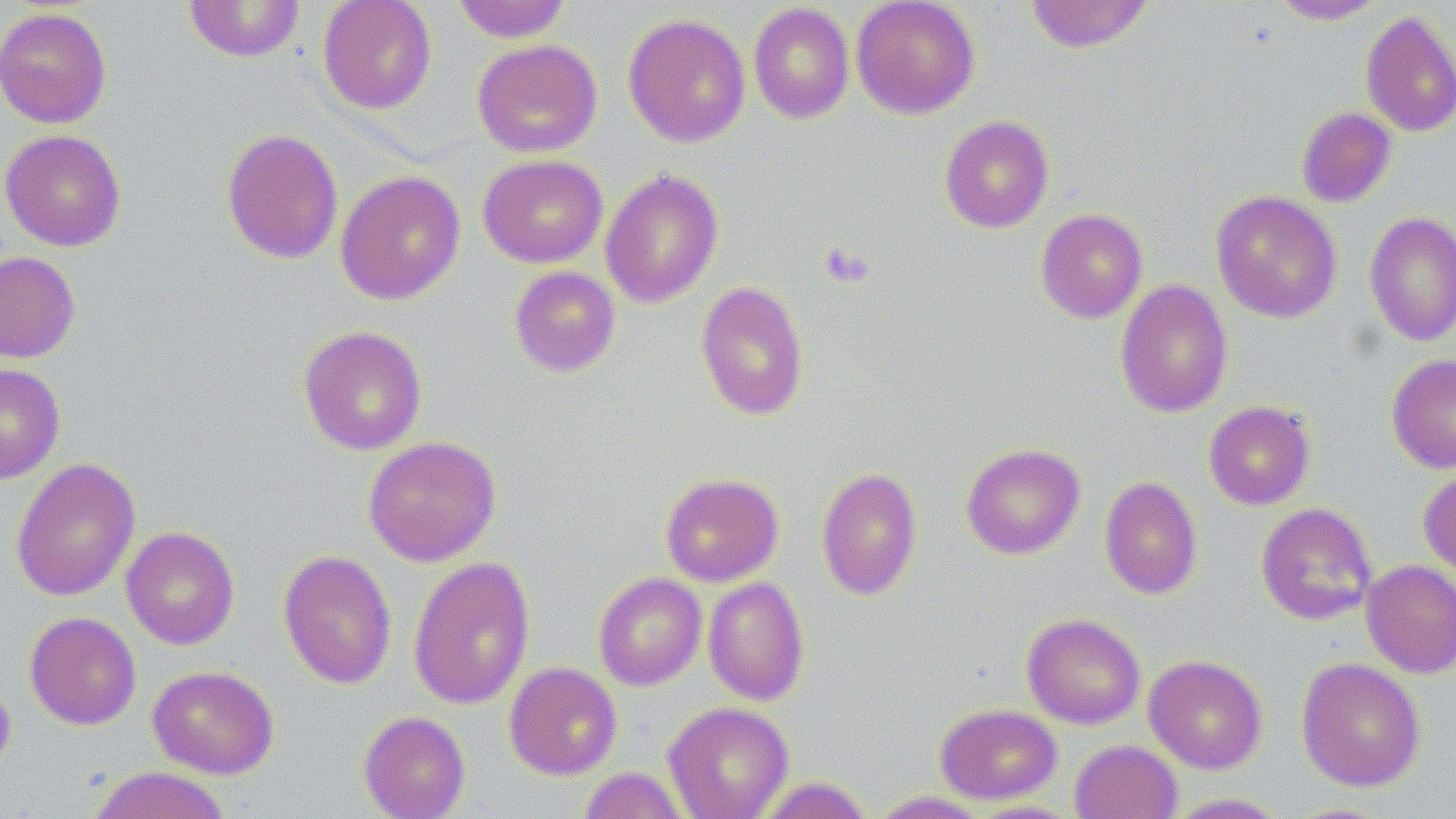
slide_level_diagnosis: negative for blood parasites
uninfected_red_blood_cell_locations: 'approximate bounding boxes as named x1/y1/x2/y2 corners in pixels: (x1=317, y1=0, x2=438, y2=114), (x1=450, y1=0, x2=572, y2=42), (x1=850, y1=0, x2=981, y2=120), (x1=1024, y1=0, x2=1155, y2=54), (x1=1270, y1=0, x2=1387, y2=24), (x1=184, y1=1, x2=305, y2=62), (x1=748, y1=3, x2=854, y2=124), (x1=0, y1=6, x2=113, y2=129), (x1=1360, y1=9, x2=1456, y2=138), (x1=623, y1=12, x2=751, y2=148), (x1=471, y1=39, x2=603, y2=158), (x1=1296, y1=106, x2=1397, y2=207), (x1=938, y1=115, x2=1055, y2=234), (x1=221, y1=128, x2=344, y2=265), (x1=0, y1=129, x2=127, y2=252), (x1=477, y1=154, x2=609, y2=269), (x1=600, y1=168, x2=724, y2=309), (x1=335, y1=170, x2=466, y2=305), (x1=1211, y1=190, x2=1342, y2=324), (x1=1035, y1=208, x2=1148, y2=324), (x1=1364, y1=211, x2=1456, y2=346), (x1=0, y1=251, x2=81, y2=363), (x1=508, y1=266, x2=621, y2=378), (x1=1114, y1=279, x2=1234, y2=418), (x1=695, y1=280, x2=810, y2=421), (x1=298, y1=325, x2=428, y2=456), (x1=1386, y1=354, x2=1456, y2=473), (x1=0, y1=363, x2=66, y2=484), (x1=1203, y1=401, x2=1316, y2=510), (x1=362, y1=435, x2=502, y2=566), (x1=961, y1=443, x2=1086, y2=560), (x1=10, y1=458, x2=141, y2=602), (x1=815, y1=466, x2=923, y2=601), (x1=1418, y1=468, x2=1456, y2=582), (x1=660, y1=472, x2=784, y2=587), (x1=1099, y1=475, x2=1203, y2=600), (x1=1256, y1=503, x2=1377, y2=626), (x1=120, y1=526, x2=240, y2=650), (x1=277, y1=549, x2=397, y2=690), (x1=408, y1=556, x2=536, y2=710), (x1=1361, y1=560, x2=1456, y2=678), (x1=593, y1=572, x2=707, y2=691), (x1=702, y1=577, x2=810, y2=706), (x1=24, y1=611, x2=141, y2=730), (x1=1021, y1=612, x2=1146, y2=729), (x1=1143, y1=654, x2=1268, y2=774), (x1=1296, y1=657, x2=1426, y2=792), (x1=504, y1=661, x2=623, y2=780), (x1=147, y1=664, x2=280, y2=779), (x1=0, y1=676, x2=16, y2=782), (x1=663, y1=702, x2=794, y2=819), (x1=935, y1=703, x2=1062, y2=804), (x1=357, y1=710, x2=471, y2=818), (x1=1069, y1=739, x2=1182, y2=819), (x1=85, y1=766, x2=234, y2=819), (x1=577, y1=767, x2=691, y2=819), (x1=754, y1=777, x2=875, y2=818), (x1=868, y1=791, x2=992, y2=818), (x1=1162, y1=792, x2=1291, y2=818)'
image_size: 1456×819 pixels
stain: May-Grünwald-Giemsa
preparation: thin blood film
magnification: 1000x
modality: light microscopy
field_of_view: one of a larger specimen